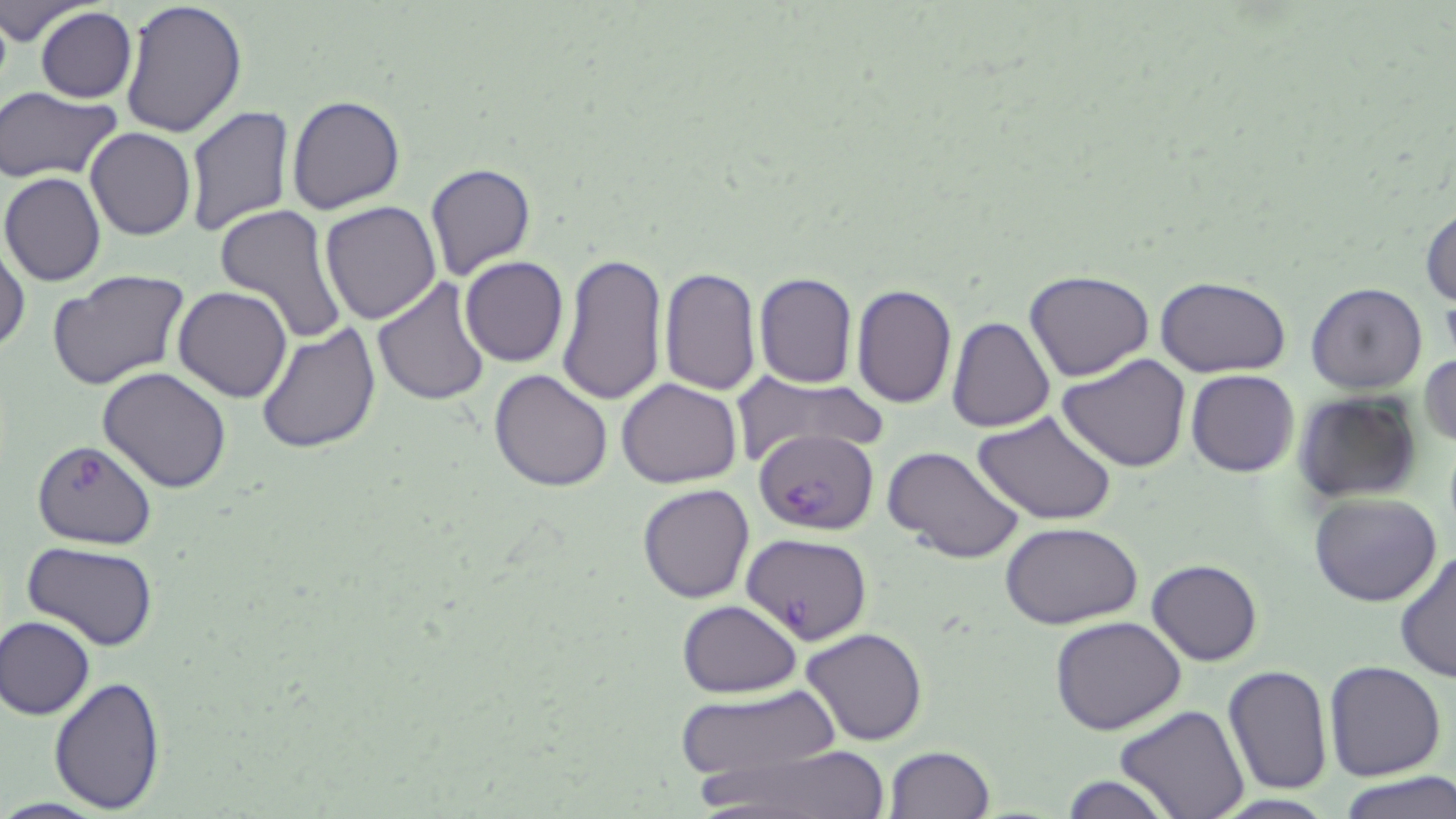
slide-level diagnosis = Plasmodium falciparum
uninfected red blood cell locations = approximate bounding boxes as (x1,y1)-(x2,y2) corner pairs in pixels: (120,0)-(248,139), (2,2)-(90,46), (34,8)-(137,103), (0,89)-(123,184), (286,95)-(404,214), (184,106)-(295,239), (85,126)-(195,241), (424,164)-(536,281), (2,172)-(106,286), (319,202)-(441,324), (214,204)-(347,342), (1421,204)-(1455,307), (0,242)-(30,355), (556,252)-(667,406), (459,256)-(568,367), (658,268)-(761,395), (46,269)-(192,392), (1024,269)-(1154,382), (754,273)-(858,388), (1155,276)-(1292,378), (371,279)-(491,405), (1306,283)-(1428,394), (850,284)-(956,409), (173,286)-(291,402), (946,315)-(1055,432), (257,322)-(383,453), (1418,350)-(1456,449), (1057,353)-(1192,475), (99,367)-(232,493), (729,368)-(888,471), (490,369)-(613,492), (1187,370)-(1299,476), (617,378)-(742,488), (1293,392)-(1422,503), (972,410)-(1118,529), (884,445)-(1024,567), (638,483)-(754,602), (1308,492)-(1442,607), (1001,522)-(1142,632), (21,542)-(156,651), (1395,548)-(1456,686), (1147,559)-(1262,667), (678,601)-(801,697), (1,616)-(95,720), (1049,616)-(1188,735), (801,627)-(928,747), (1323,660)-(1445,781), (1224,664)-(1334,797), (48,675)-(165,815), (671,685)-(840,783), (1115,705)-(1250,818), (700,745)-(890,819), (884,746)-(994,818), (1340,771)-(1456,819), (1057,775)-(1175,818)
field of view = single
preparation = thin blood film
magnification = 1000x
image size = 1456×819 pixels
modality = optical microscopy
Plasmodium falciparum-infected red blood cell locations = approximate bounding boxes as (x1,y1)-(x2,y2) corner pairs in pixels: (756,429)-(878,535), (32,440)-(156,549), (741,532)-(873,644)
stain = May-Grünwald-Giemsa